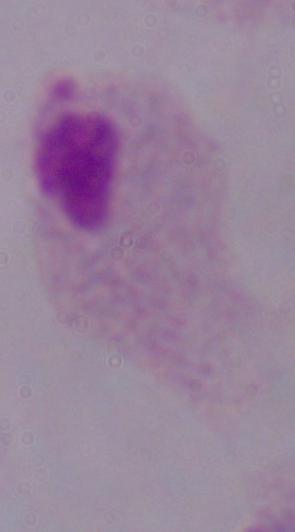

Summary:
  - Modality: photomicrograph
  - Magnification: 1000x
  - Identification: trichomonad